Classify this cell by malaria status.
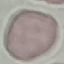
It is uninfected.

stain = Giemsa
preparation = thin blood film
image type = automatically extracted cell patch, resized to 64 × 64 pixels
capture = smartphone camera at the microscope eyepiece